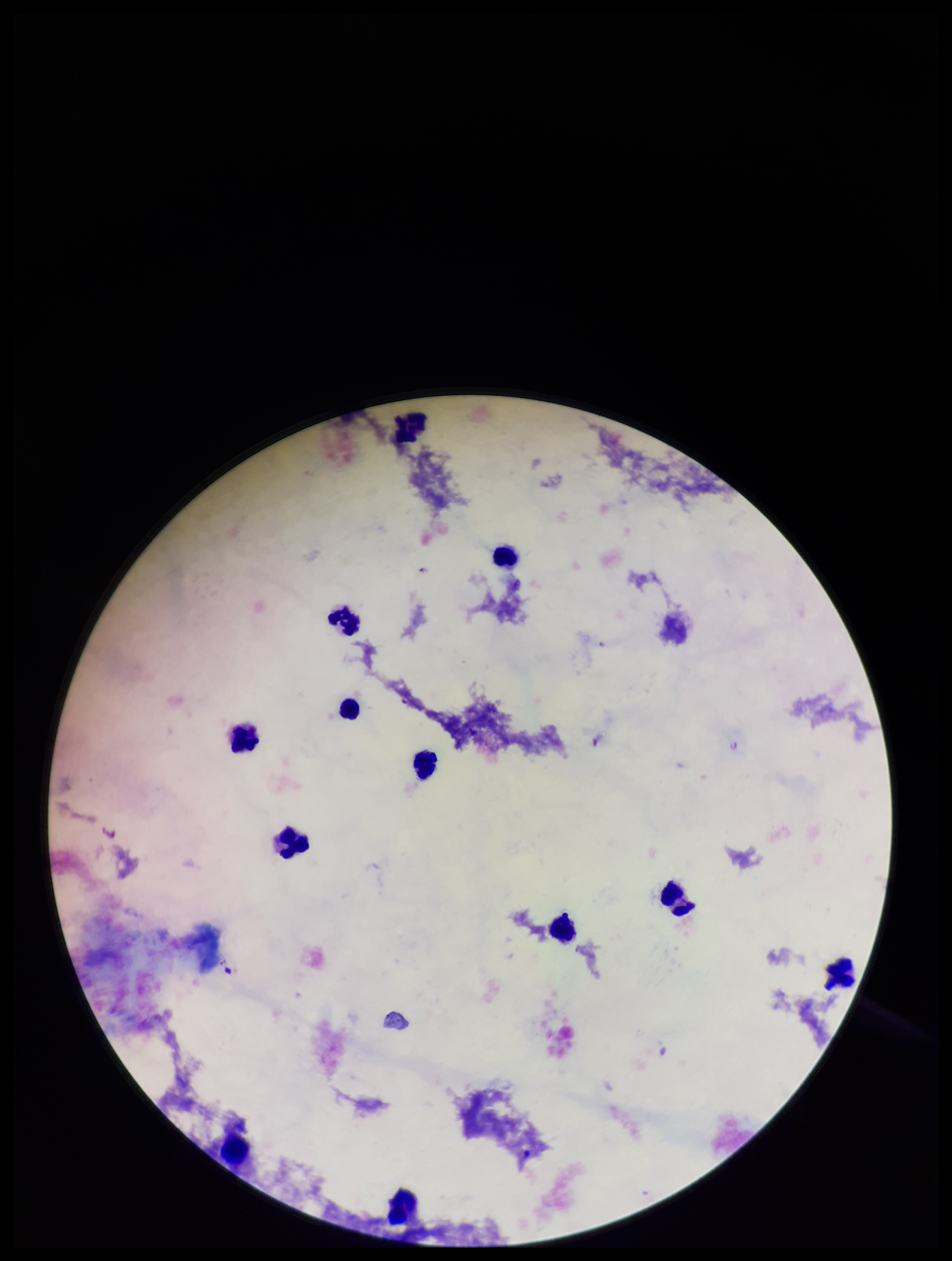 Patient malaria status: negative. Leukocyte count: 12. Parasite count: 0. Plasmodium parasites: none seen. Single field of view. Preparation: thick blood smear. Image is 952×1261 pixels. Photographed through the microscope eyepiece with a smartphone camera. Stained with Giemsa.